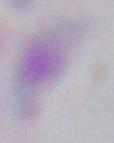
magnification = 1000x
modality = micrograph
identification = Toxoplasma gondii